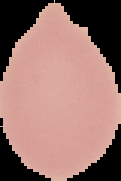
Summary:
  - Image size: 121×181 pixels
  - Image type: segmented cell region with the area outside set to black
  - Result: no Plasmodium parasites detected
  - Preparation: thin blood smear